Identify the cell.
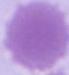

An erythrocyte.

Photomicrograph. Captured at 1000x magnification.